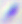
{
  "modality": "photomicrograph",
  "identification": "Toxoplasma gondii",
  "magnification": "400x"
}